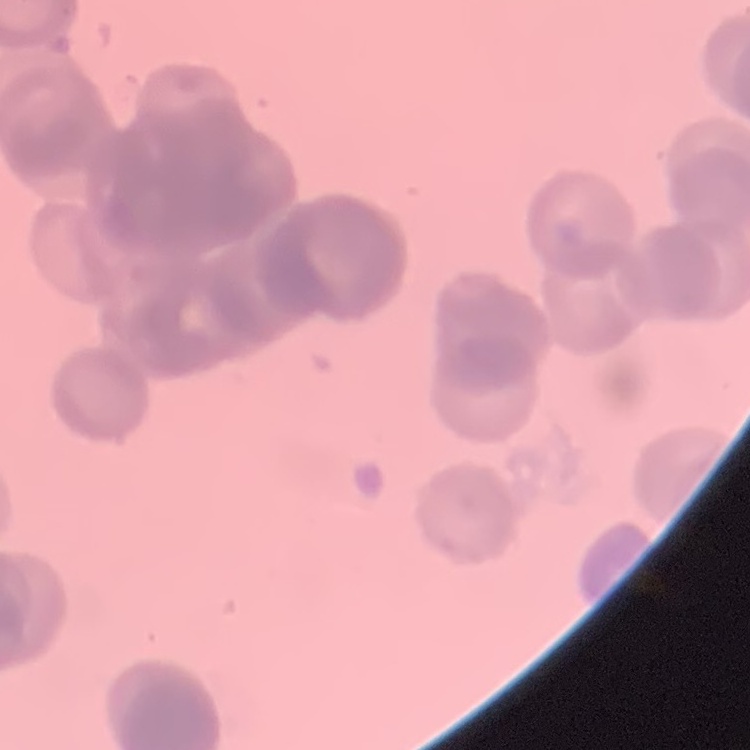

red_blood_cell_morphology: rouleaux formation
image_type: square crop of a larger photomicrograph
preparation: thin peripheral smear
stain: Field's or Giemsa